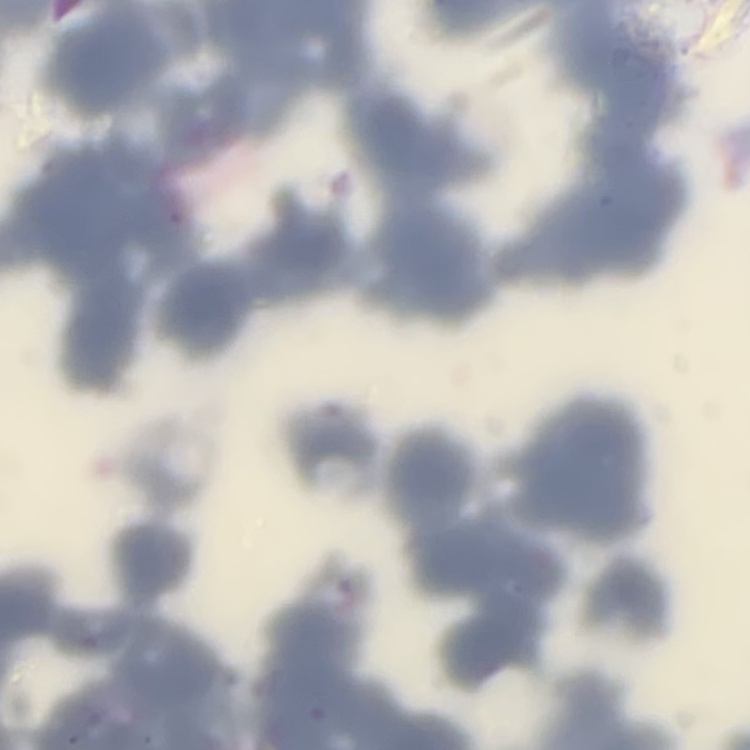

erythrocyte_morphology: rouleaux formation
image_type: square crop of a larger photomicrograph
stain: Field's or Giemsa
preparation: thin blood smear